Assess for parasitized red blood cells.
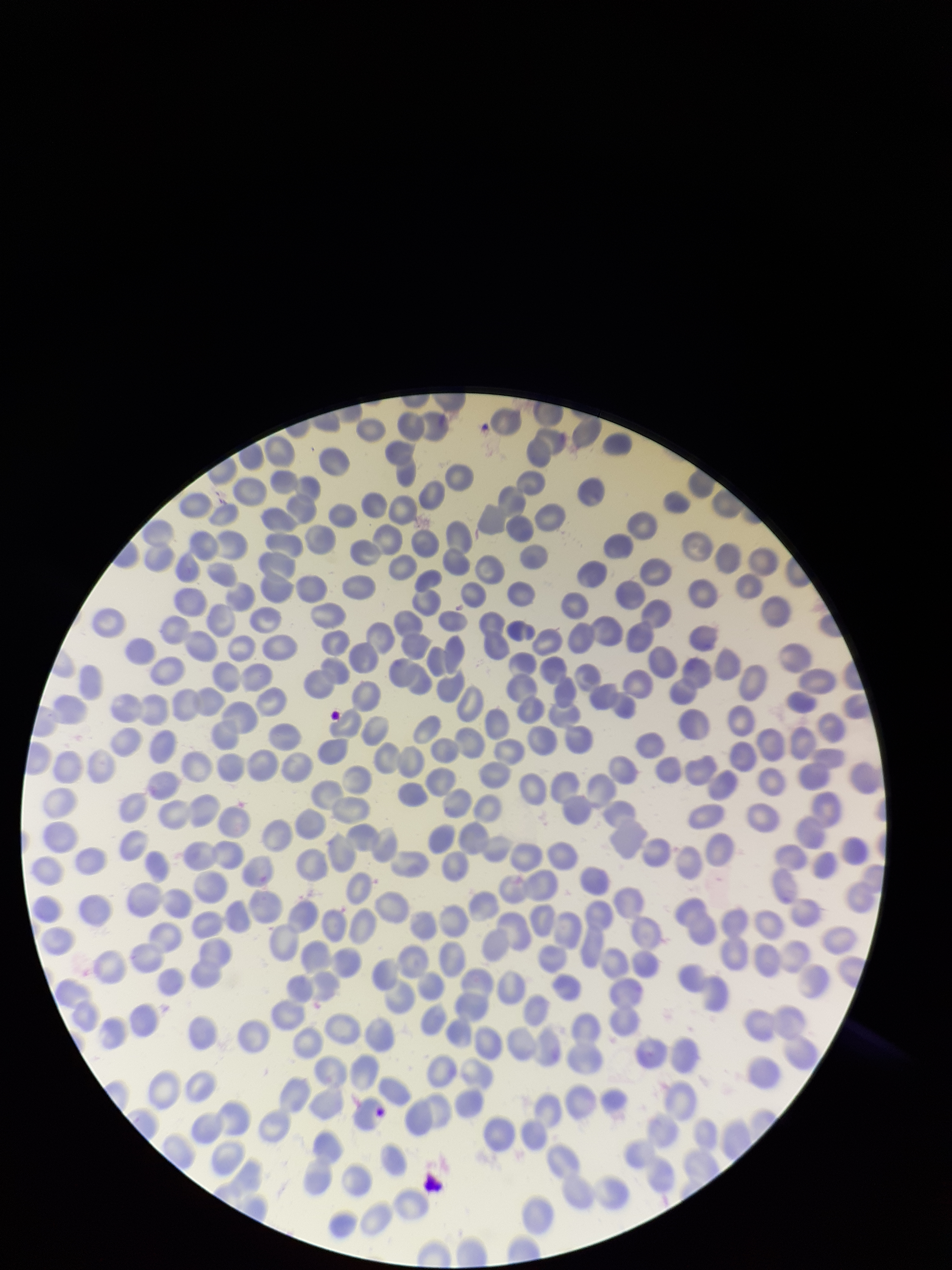
None seen.

{
  "stain": "Giemsa",
  "preparation": "thin smear",
  "parasitized_red_blood_cell_count": 0,
  "image_size": "952×1270 pixels",
  "field_of_view": "single",
  "red_blood_cell_count": 320,
  "patient_malaria_status": "negative",
  "capture": "smartphone photograph through the microscope eyepiece"
}